Locate malaria parasites and leukocytes.
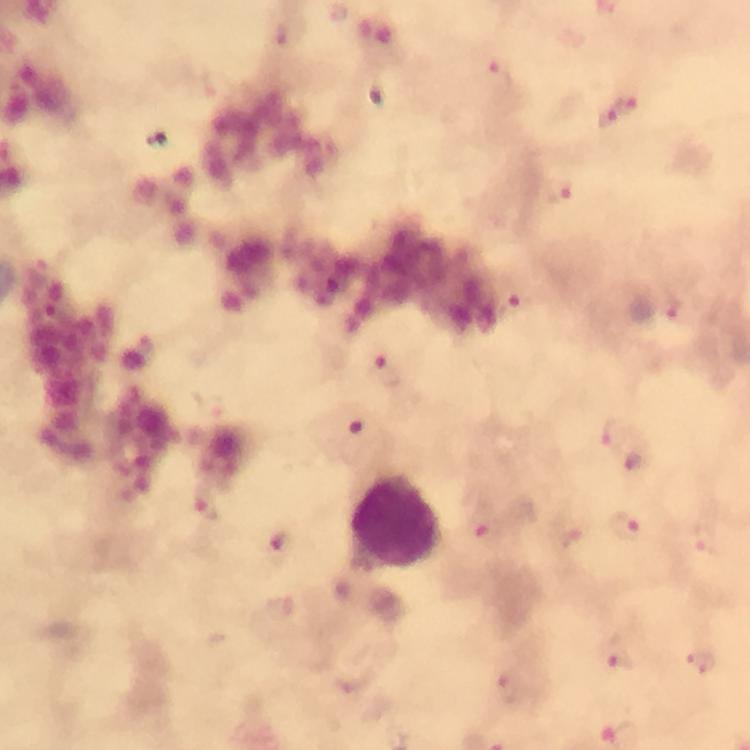
Approximate centers as (x, y) in pixels.
Malaria parasites: (497, 77), (626, 106), (605, 116), (558, 190), (519, 305), (667, 310), (388, 372), (610, 433), (634, 457), (206, 508), (482, 526), (625, 527), (574, 530), (707, 542), (618, 655), (702, 663), (507, 685).
Leukocytes: (396, 518).

capture = smartphone mounted on the microscope
image size = 750×750 pixels
immersion oil = applied
cropped from = one field of view
magnification = 100x
preparation = thick smear
context = from a malaria diagnostic workup
stain = Giemsa